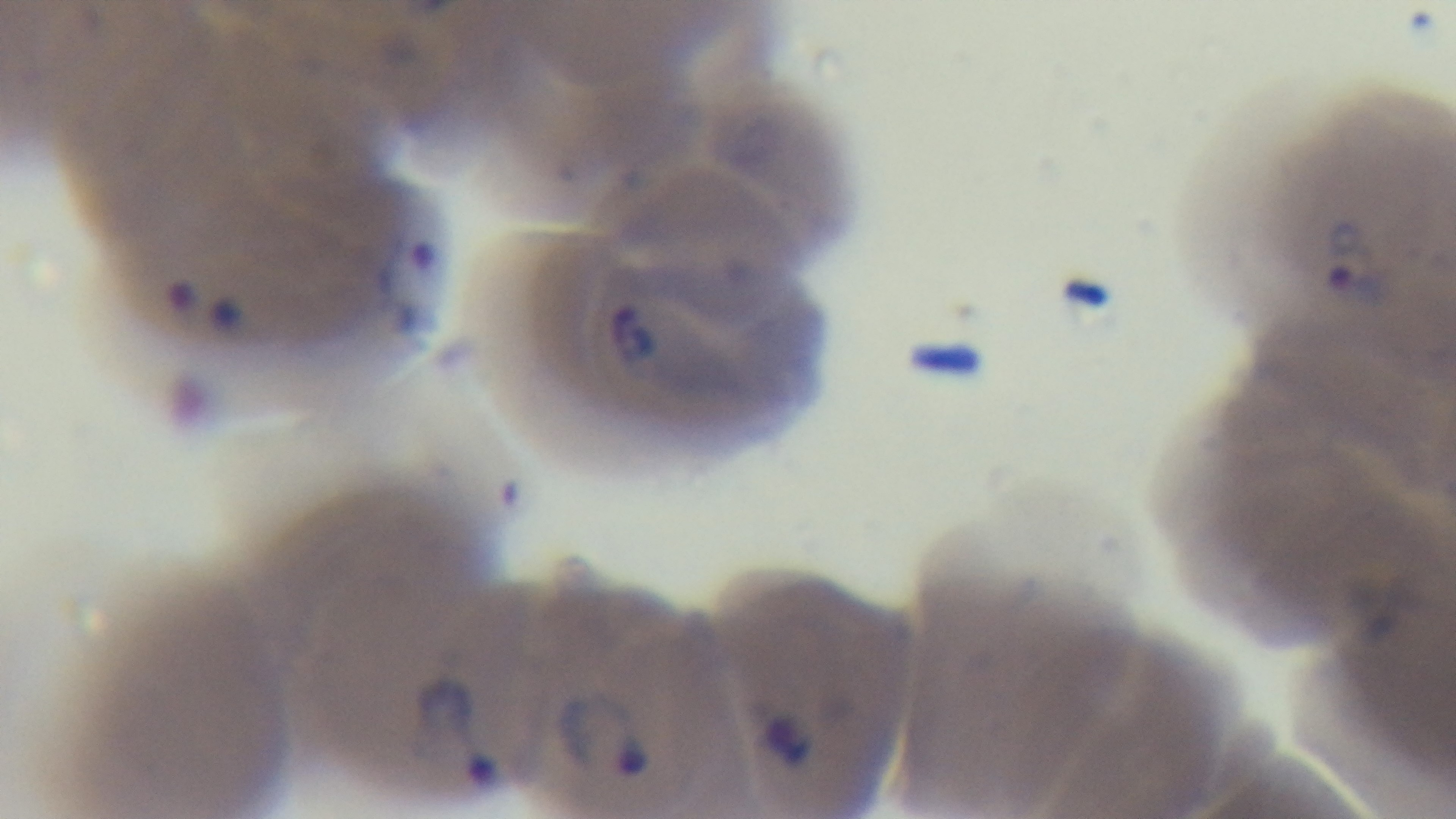
Summary:
  - Malaria status: positive
  - Modality: light microscopy
  - Capture: mounted 4K digital camera
  - Preparation: thin blood film
  - Field of view: single
  - Stain: Giemsa
  - Objective: 100x oil immersion